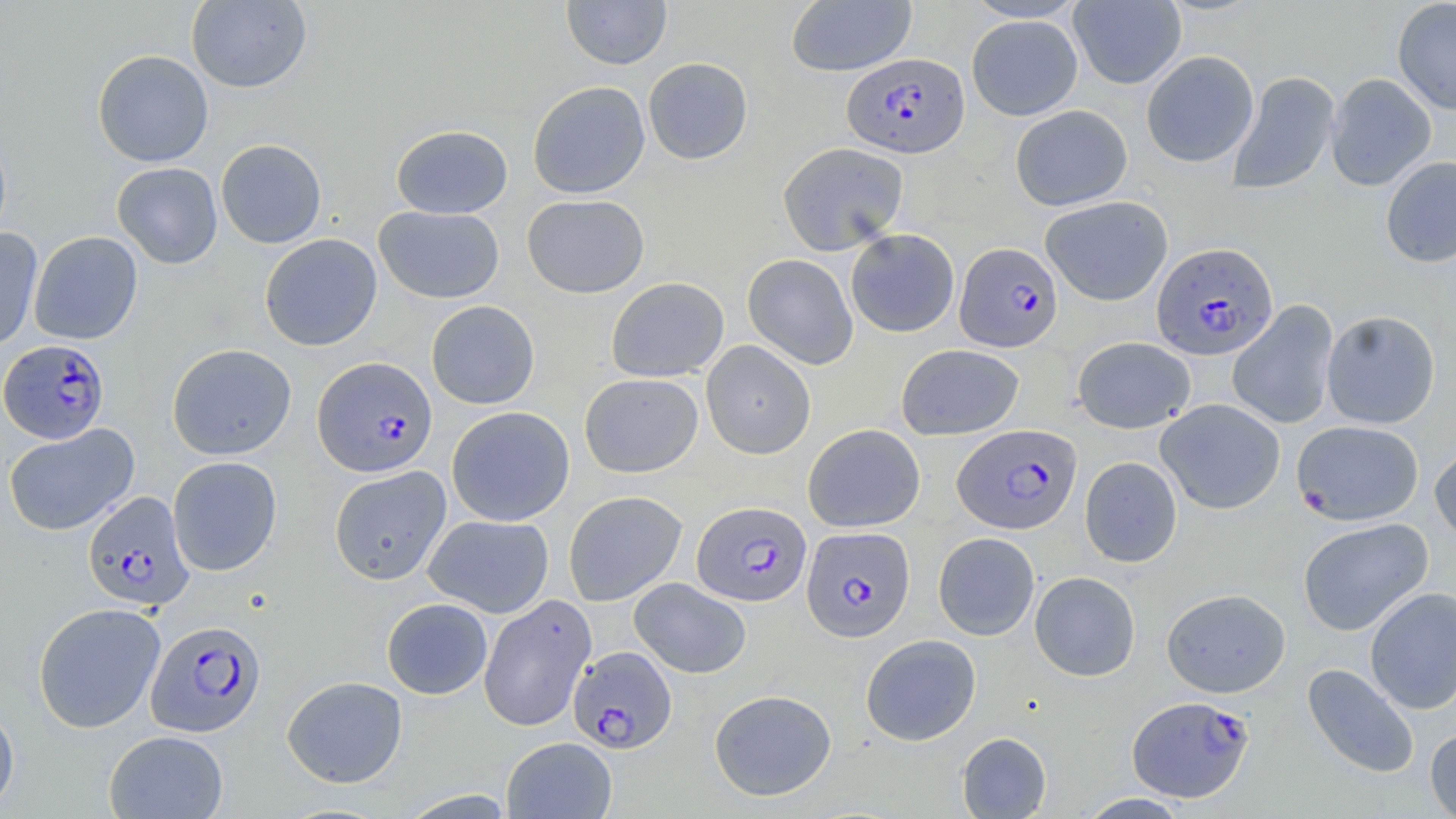
Approximate bounding boxes as (x1,y1)-(x2,y2) corner pairs in pixels. Uninfected red blood cell locations: (561,0)-(672,69), (962,0)-(1088,23), (1392,0)-(1456,114), (186,1)-(311,93), (785,1)-(917,76), (1068,1)-(1186,90), (966,15)-(1083,121), (92,49)-(213,168), (1141,50)-(1259,167), (642,57)-(753,165), (1226,71)-(1341,195), (1326,73)-(1436,191), (527,81)-(650,199), (1010,105)-(1132,211), (391,125)-(513,219), (215,139)-(327,248), (778,142)-(908,255), (1380,156)-(1456,267), (112,162)-(223,269), (522,194)-(649,298), (1041,195)-(1173,306), (374,205)-(504,303), (0,227)-(43,351), (845,229)-(959,337), (29,231)-(142,345), (260,234)-(382,351), (742,253)-(858,369), (606,277)-(729,382), (426,300)-(540,409), (1227,300)-(1339,430), (1321,310)-(1440,429), (1072,336)-(1196,433), (701,341)-(816,459), (167,343)-(296,460), (896,343)-(1025,440), (579,373)-(703,477), (1155,398)-(1285,515), (446,406)-(575,526), (1291,420)-(1424,525), (3,423)-(139,536), (803,423)-(925,532), (1430,440)-(1456,545), (167,456)-(282,576), (1079,456)-(1182,567), (329,466)-(452,585), (563,491)-(687,606), (424,514)-(554,617), (1297,517)-(1433,636), (933,532)-(1040,640), (1029,571)-(1141,681), (629,577)-(751,679), (1365,586)-(1456,715), (1161,588)-(1290,698), (478,594)-(596,731), (382,598)-(493,699), (33,602)-(166,733), (861,634)-(981,746), (1302,663)-(1419,779), (282,675)-(407,788), (709,688)-(836,801), (0,701)-(19,814), (1425,725)-(1456,819), (104,730)-(229,818), (956,732)-(1051,818), (501,736)-(617,818), (1077,792)-(1192,818). Plasmodium falciparum-infected red blood cell locations: (842,53)-(970,158), (955,242)-(1063,352), (1152,242)-(1278,361), (0,341)-(110,444), (312,356)-(438,477), (953,424)-(1082,534), (83,491)-(194,611), (692,501)-(811,606), (801,526)-(914,642), (146,619)-(266,737), (569,646)-(676,753), (1127,695)-(1254,802). Slide-level diagnosis: Plasmodium falciparum. Captured at 1000x magnification. Image is 1456×819 pixels. Thin blood smear. Single field of view. Optical microscopy. May-Grünwald-Giemsa-stained preparation.